Assess this cell for malaria.
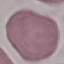

Uninfected.

capture: smartphone through the microscope eyepiece
stain: Giemsa
image_type: cell patch, automatically extracted from a larger field of view and resized to 64 × 64 pixels
preparation: thin smear